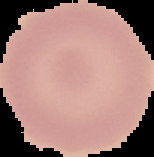
result = no malaria parasites detected
image size = 154×157 pixels
image type = cell region segmented out of the field of view; surrounding area masked to black
preparation = thin blood film